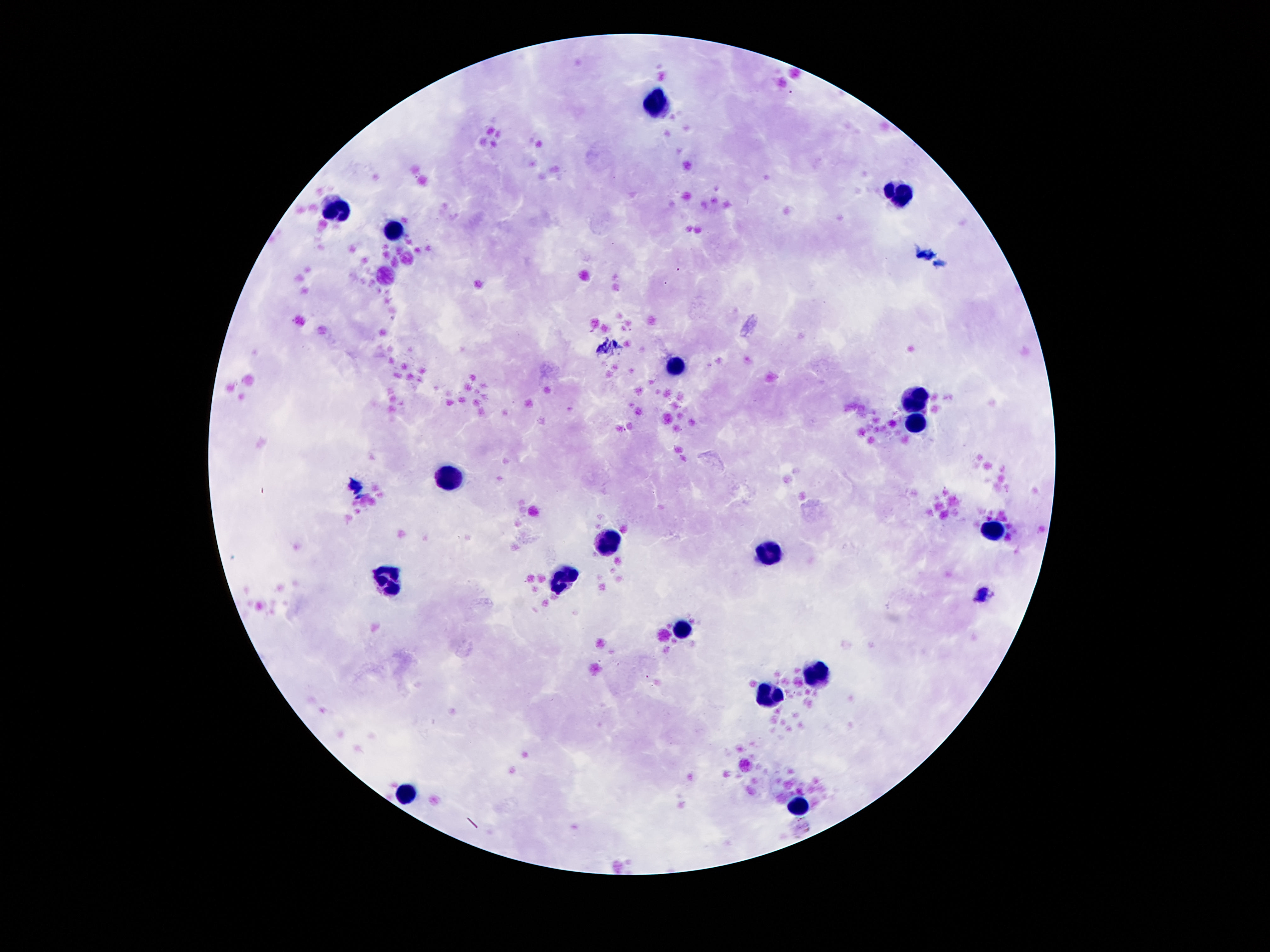
Approximate centers as (x, y) in pixels. Leukocyte locations: (657, 98), (898, 196), (337, 207), (396, 231), (676, 369), (917, 400), (914, 420), (452, 476), (996, 527), (606, 541), (769, 551), (561, 580), (390, 585), (682, 627), (816, 672), (772, 695), (407, 791), (800, 805). 100x magnification. Patient malaria status: uninfected. Thick blood film. Giemsa-stained preparation. One field from this slide. Smartphone photograph taken through the microscope eyepiece. Image is 1270×952 pixels.